Give the position of every leukocyte visible.
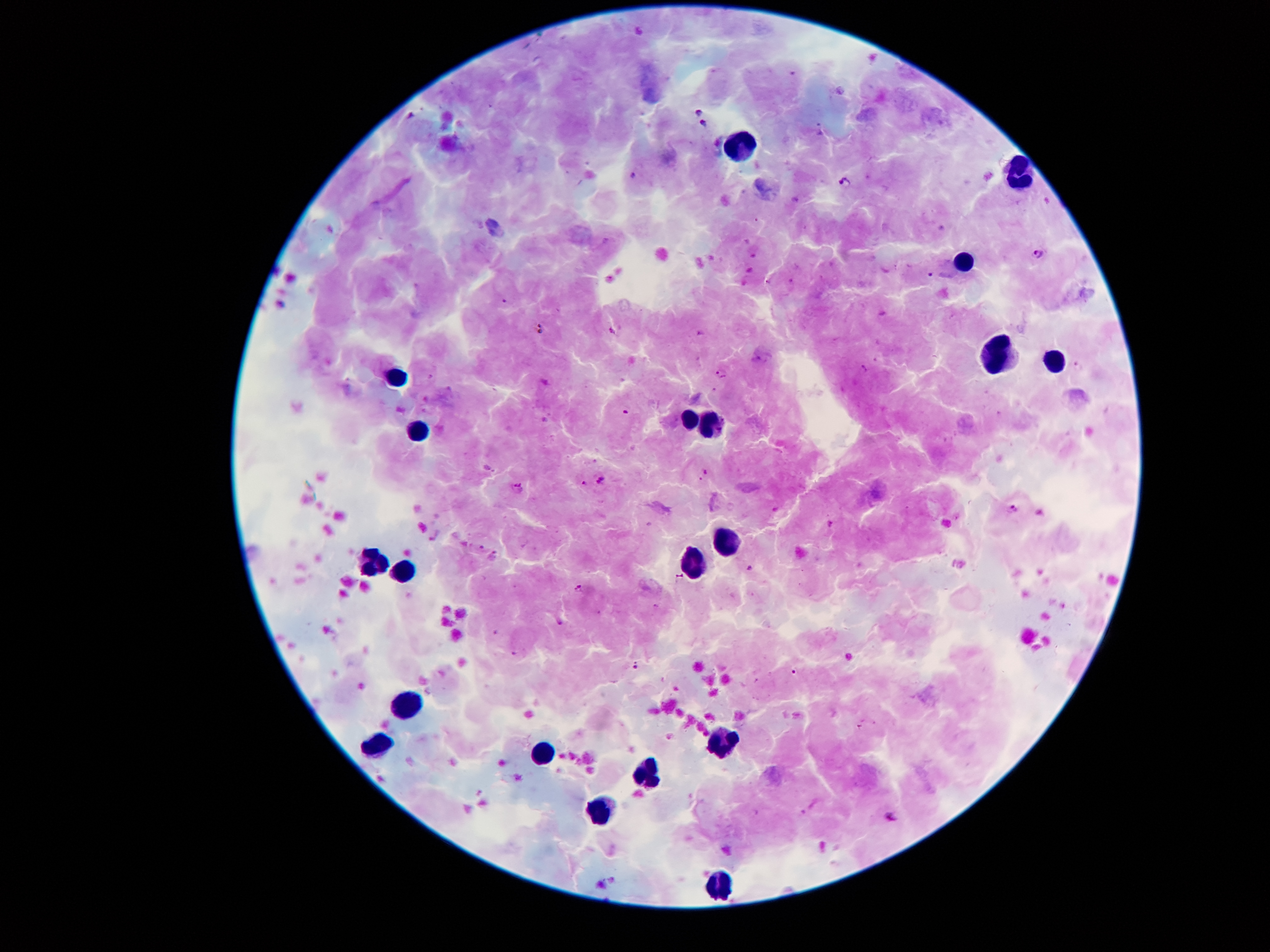
Approximate centers as [x, y] in pixels.
Leukocytes: [741, 144], [1018, 171], [963, 261], [998, 356], [1055, 362], [396, 386], [685, 417], [715, 425], [423, 429], [726, 538], [694, 557], [371, 563], [401, 564], [404, 696], [376, 743], [724, 745], [540, 754], [641, 772], [602, 810], [717, 890].

Summary:
  - Malaria parasite locations: [640, 30], [840, 89], [697, 108], [410, 113], [705, 123], [634, 174], [845, 181], [1040, 253], [931, 276], [544, 329], [722, 374], [626, 409], [706, 476], [583, 480], [601, 481], [517, 488], [1014, 509], [483, 547], [495, 555], [750, 566], [679, 577], [577, 587], [559, 623], [636, 666], [795, 672]
  - Patient malaria status: infected with Plasmodium falciparum
  - Field of view: single
  - Magnification: 100x
  - Image size: 1270×952 pixels
  - Stain: Giemsa
  - Capture: smartphone through the microscope eyepiece
  - Preparation: thick blood film